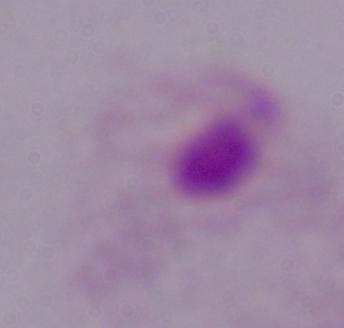

identification = trichomonad
modality = photomicrograph
magnification = 1000x